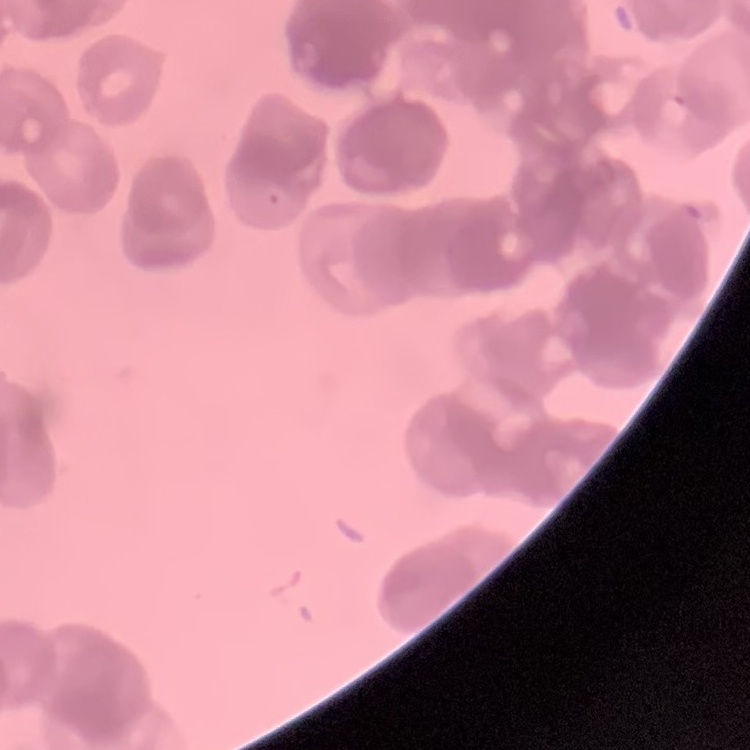

The erythrocytes show rouleaux formation. Thin blood smear. Field's or Giemsa stain. Square crop of a larger photomicrograph.